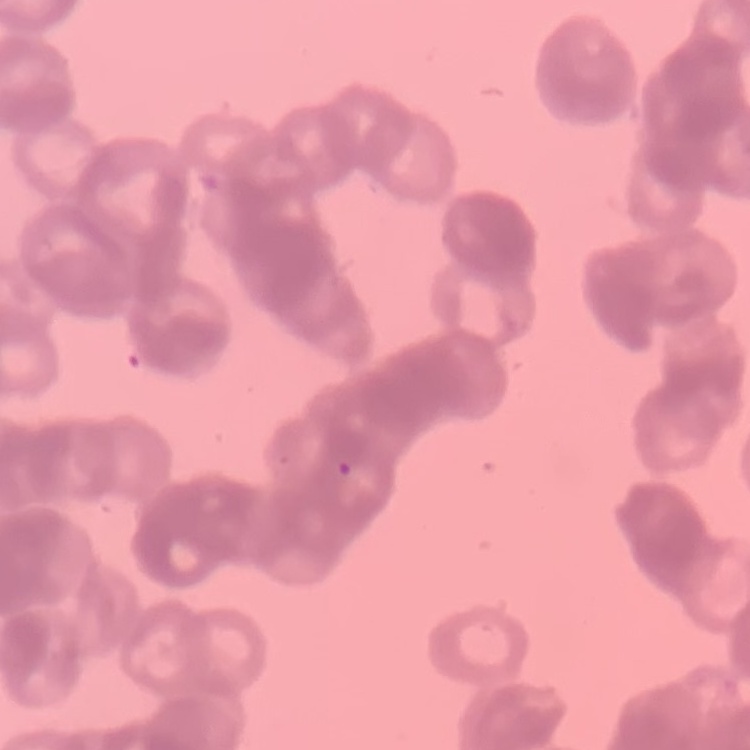

Summary:
  - Red blood cell morphology: rouleaux formation
  - Image type: square crop of a larger photomicrograph
  - Preparation: thin blood smear
  - Stain: Field's or Giemsa